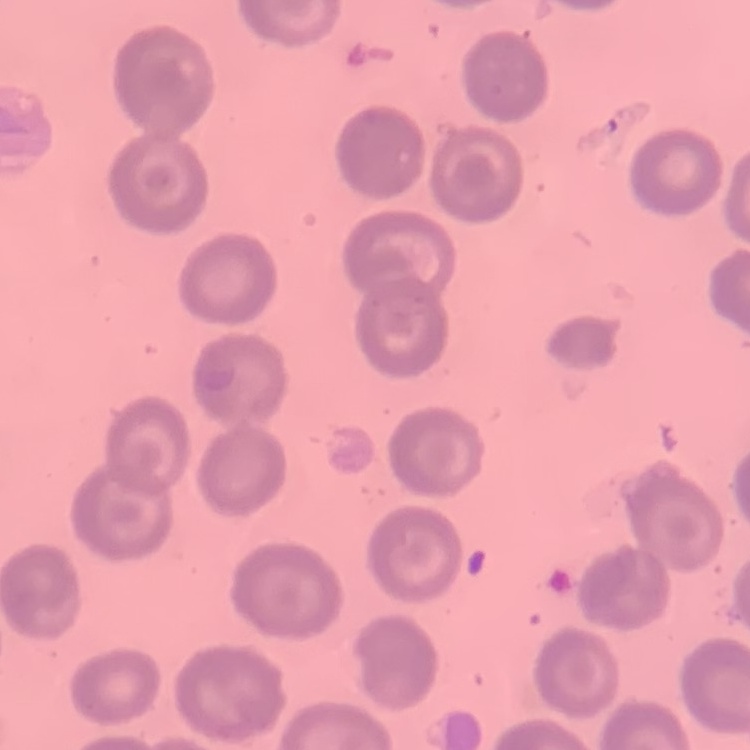

Summary:
  - Red blood cell morphology: no rouleaux formation
  - Stain: Field's or Giemsa
  - Image type: one tile cut from a larger photomicrograph
  - Preparation: thin peripheral smear